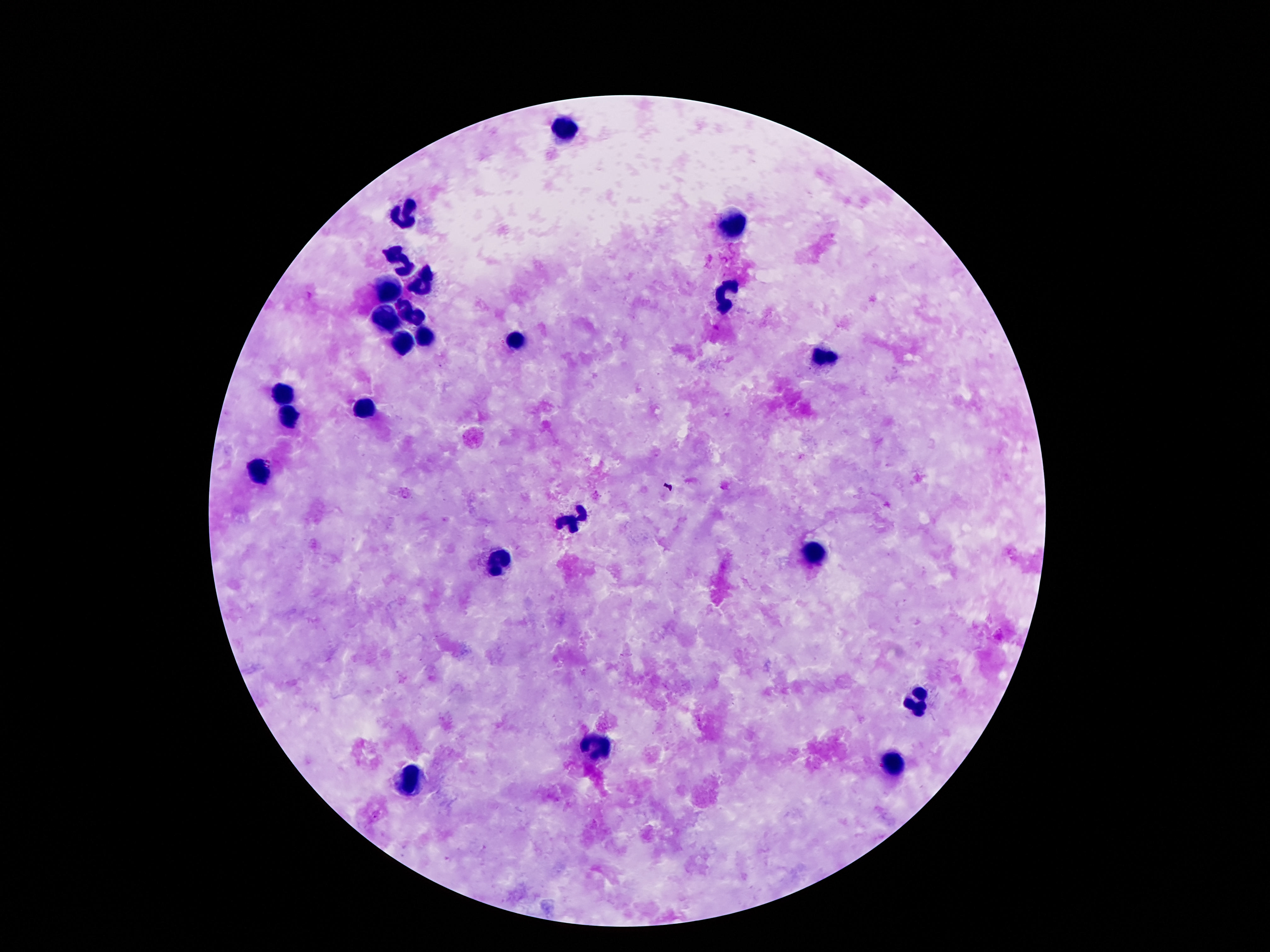 Approximate centers as (x, y) in pixels. Leukocyte locations: (566, 128), (407, 210), (732, 223), (398, 260), (427, 280), (391, 289), (725, 294), (407, 311), (385, 313), (424, 336), (407, 342), (513, 342), (822, 359), (283, 393), (365, 406), (290, 417), (263, 474), (572, 519), (813, 554), (497, 563), (915, 698), (597, 747), (895, 762), (409, 782). Image is 1270×952 pixels. Patient malaria status: not infected. Giemsa stain. Thick blood smear. Smartphone photograph taken through the microscope eyepiece. One field from this slide. 100x magnification.